Assess for Plasmodium parasites.
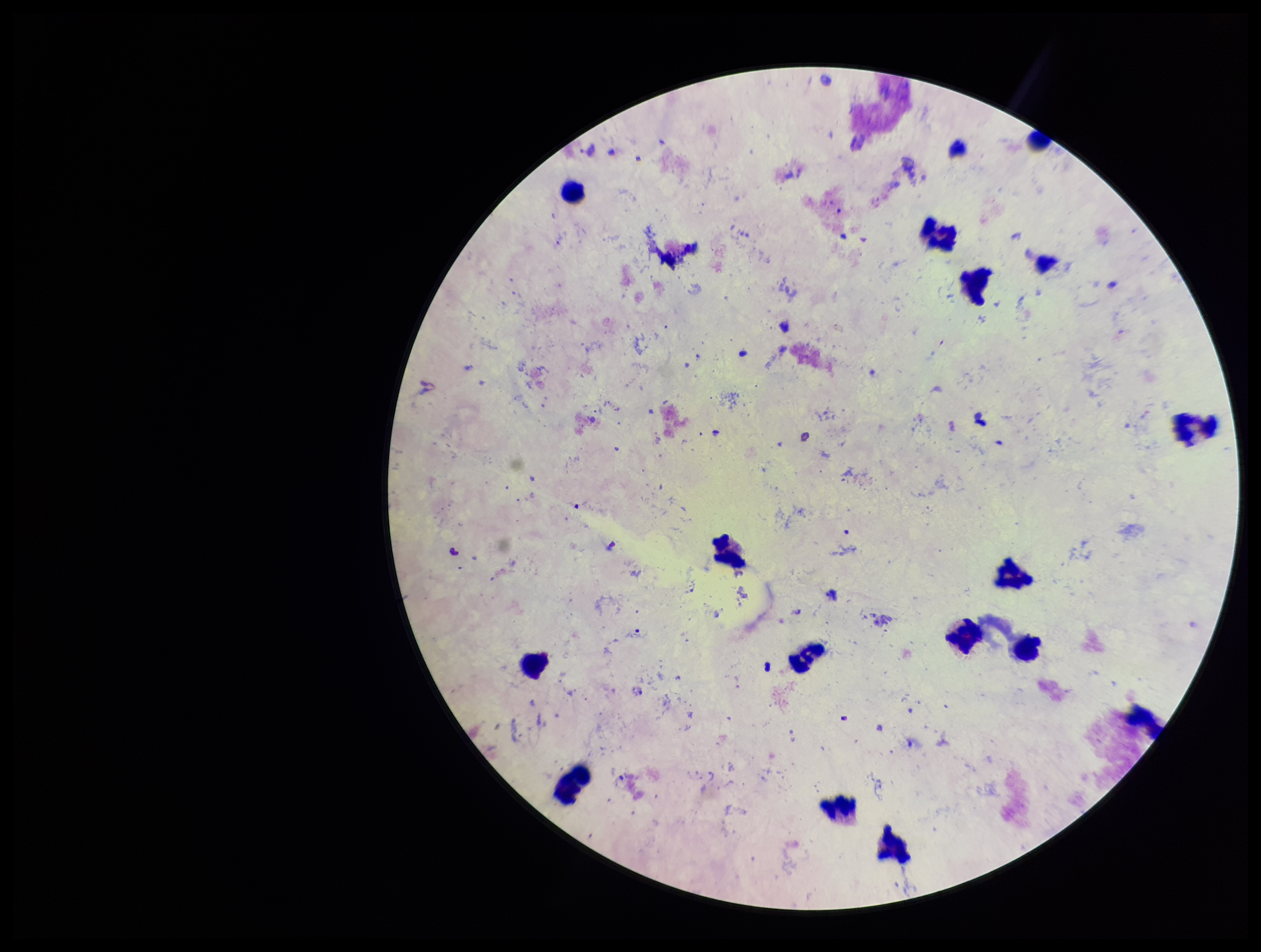
None seen.

stain = Giemsa
parasite count = 0
field of view = one from this slide
preparation = thick
image size = 1261×952 pixels
leukocyte count = 14
capture = smartphone photograph through the microscope eyepiece
patient malaria status = negative